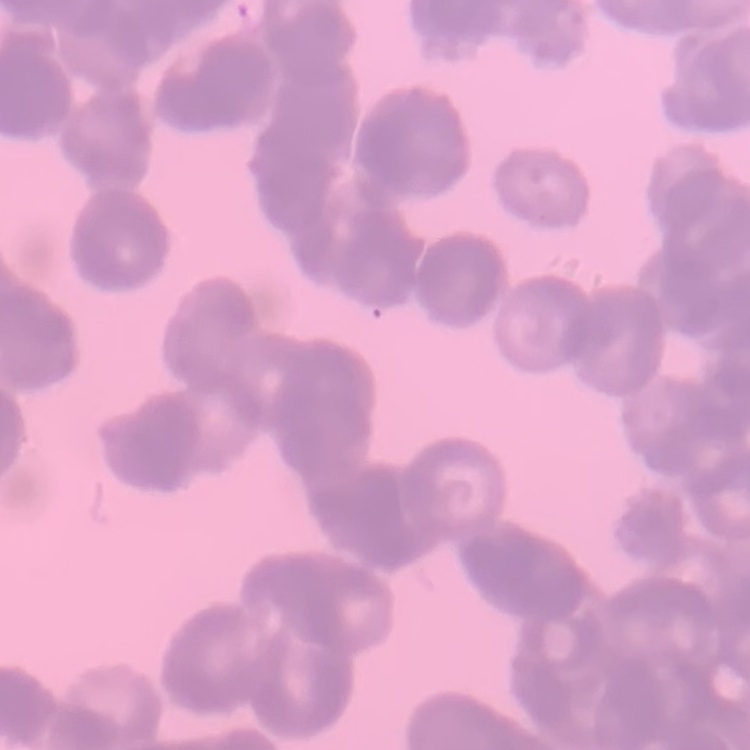
erythrocyte morphology = rouleaux formation
preparation = thin blood smear
image type = one tile cut from a larger photomicrograph
stain = Field's or Giemsa